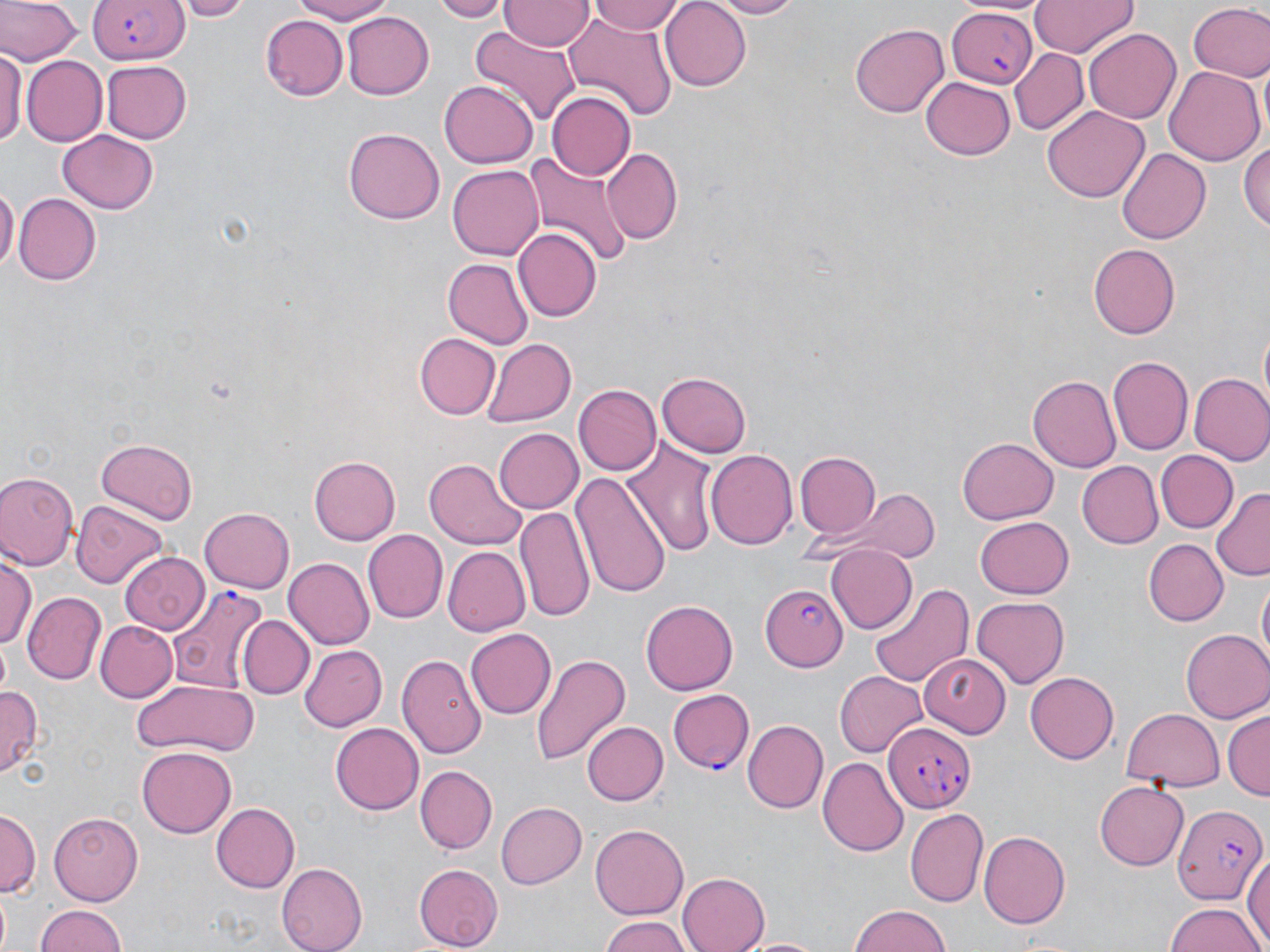
slide-level diagnosis = Plasmodium falciparum
preparation = thin blood smear
Plasmodium falciparum-infected red blood cell locations = approximate bounding boxes as (x1, y1, x2, y2) in pixels: (87, 0, 186, 64), (946, 5, 1037, 89), (759, 582, 848, 672), (167, 586, 267, 694), (667, 689, 754, 774), (882, 722, 975, 814), (1174, 802, 1268, 905)
field of view = single
stain = May-Grünwald-Giemsa
image size = 1270×952 pixels
uninfected red blood cell locations = approximate bounding boxes as (x1, y1, x2, y2) in pixels: (0, 0, 79, 66), (173, 0, 253, 21), (285, 0, 403, 24), (433, 0, 507, 21), (500, 0, 593, 50), (586, 0, 686, 35), (660, 0, 752, 90), (705, 0, 803, 17), (1030, 0, 1138, 57), (1187, 3, 1270, 82), (340, 11, 433, 100), (559, 14, 678, 118), (263, 15, 348, 101), (851, 24, 948, 117), (469, 28, 582, 126), (1083, 28, 1182, 125), (1008, 47, 1088, 135), (1, 49, 27, 150), (21, 56, 106, 146), (103, 61, 192, 144), (1165, 66, 1265, 165), (921, 77, 1015, 159), (440, 82, 538, 169), (547, 91, 637, 182), (1043, 106, 1148, 203), (343, 127, 444, 224), (57, 132, 158, 213), (1243, 139, 1270, 234), (601, 148, 684, 246), (1118, 149, 1210, 243), (524, 150, 634, 271), (450, 164, 545, 260), (0, 185, 17, 278), (12, 191, 100, 284), (514, 228, 600, 322), (1089, 243, 1181, 338), (440, 258, 531, 348), (413, 334, 498, 419), (481, 338, 577, 427), (1107, 357, 1193, 456), (657, 371, 752, 457), (1188, 373, 1270, 468), (1028, 375, 1120, 473), (574, 384, 659, 475), (493, 428, 584, 515), (95, 437, 199, 522), (958, 438, 1057, 524), (624, 439, 720, 559), (1156, 449, 1237, 531), (706, 450, 797, 551), (795, 452, 879, 540), (309, 455, 400, 545), (424, 459, 527, 550), (1074, 461, 1162, 549), (0, 472, 79, 571), (570, 472, 672, 599), (1211, 487, 1270, 579), (852, 488, 938, 564), (72, 500, 168, 589), (514, 504, 593, 620), (199, 507, 295, 594), (975, 517, 1074, 598), (361, 530, 447, 624), (1141, 539, 1227, 626), (824, 542, 917, 634), (441, 546, 528, 637), (2, 553, 37, 650), (122, 553, 208, 635), (285, 559, 373, 649), (1255, 574, 1269, 667), (868, 581, 972, 686), (22, 593, 105, 685), (972, 596, 1071, 687), (641, 599, 738, 696), (237, 615, 315, 700), (93, 620, 177, 702), (466, 628, 556, 719), (1182, 629, 1270, 723), (299, 645, 387, 731), (397, 653, 486, 760), (531, 653, 629, 769), (922, 655, 1006, 735), (835, 670, 928, 755), (1024, 672, 1119, 764), (132, 677, 261, 758), (0, 685, 42, 775), (1120, 708, 1226, 791), (1224, 711, 1269, 802), (582, 720, 668, 806), (742, 720, 828, 813), (330, 722, 425, 814), (137, 744, 234, 835), (819, 757, 908, 856), (414, 765, 495, 853), (1095, 779, 1189, 870), (496, 800, 585, 889), (214, 801, 301, 893), (904, 808, 988, 906), (0, 809, 40, 903), (48, 812, 145, 907), (589, 824, 690, 918), (978, 831, 1069, 930), (1242, 850, 1270, 952), (278, 863, 367, 951), (413, 865, 503, 950), (678, 871, 768, 952), (0, 888, 12, 952), (1164, 903, 1265, 951), (34, 905, 131, 952), (846, 905, 951, 950), (598, 914, 693, 952), (738, 934, 823, 952)
modality = optical microscopy
magnification = 1000x